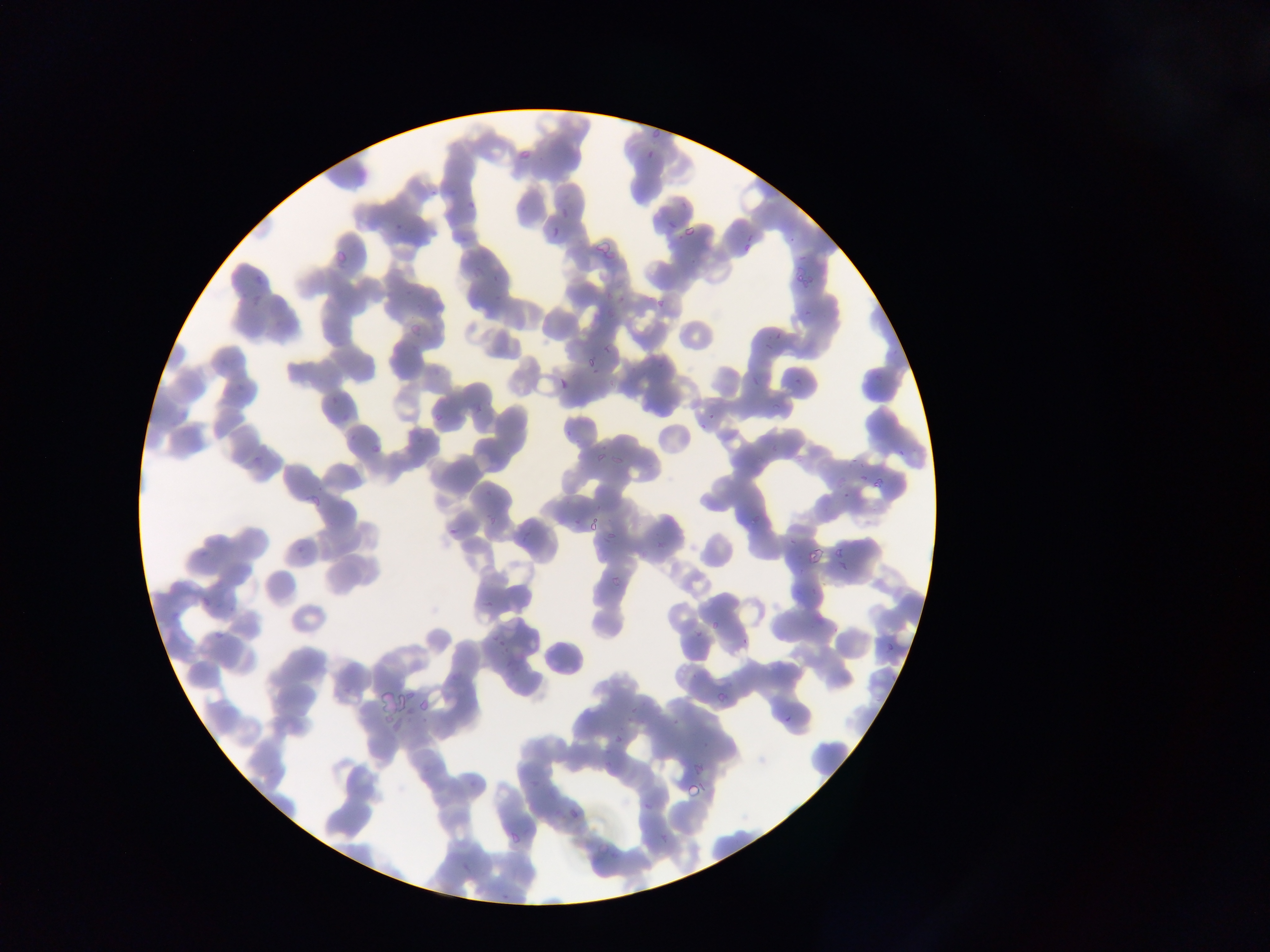
Approximate bounding boxes as [left, top, right, bottom] in pixels. Plasmodium parasite locations: [653, 128, 664, 137], [516, 152, 529, 159], [667, 219, 680, 232], [685, 224, 696, 235], [747, 232, 753, 240], [742, 244, 752, 250], [337, 249, 349, 263], [798, 255, 806, 263], [791, 271, 811, 286], [617, 294, 628, 304], [657, 300, 665, 308], [804, 309, 814, 318], [409, 324, 422, 335], [772, 332, 782, 338], [763, 341, 775, 350], [604, 342, 614, 353], [587, 356, 597, 368], [751, 373, 759, 386], [794, 374, 800, 386], [557, 378, 566, 390], [473, 396, 483, 412], [771, 400, 783, 409], [707, 411, 716, 420], [433, 414, 443, 420], [697, 420, 708, 431], [897, 448, 905, 456], [594, 451, 604, 462], [610, 454, 623, 467], [859, 473, 870, 480], [876, 473, 891, 491], [841, 490, 851, 500], [312, 494, 320, 507], [750, 508, 764, 524], [485, 513, 496, 525], [589, 518, 601, 531], [448, 528, 458, 535], [607, 528, 618, 541], [519, 529, 534, 542], [789, 537, 800, 545], [808, 546, 825, 565], [834, 546, 845, 556], [835, 559, 847, 572], [612, 575, 622, 585], [200, 597, 210, 607], [484, 600, 495, 608], [711, 618, 719, 630], [216, 631, 223, 639], [495, 633, 506, 648], [886, 637, 895, 650], [503, 645, 511, 654], [716, 690, 728, 702], [628, 704, 639, 713], [784, 714, 792, 725], [615, 735, 626, 745], [696, 764, 704, 776], [687, 783, 698, 797], [643, 801, 651, 811], [571, 809, 577, 818], [511, 831, 519, 842], [658, 833, 669, 845], [597, 842, 610, 856]. Image is 1270×952 pixels. One field of view. Photographed through a microscope with a mobile-phone camera. Thin blood smear. Collected in Ghana.